Locate and identify every blood parasite.
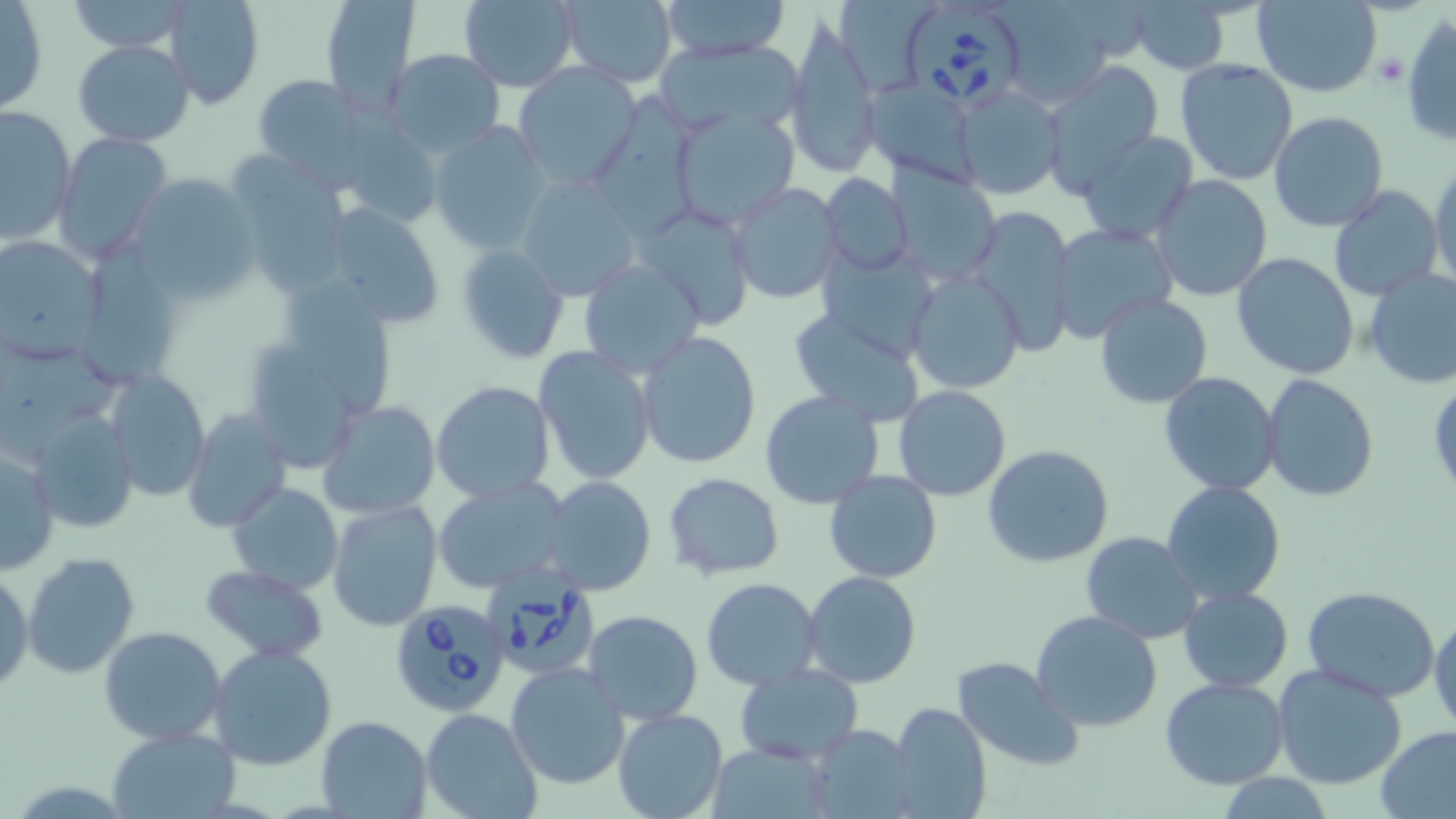
Approximate bounding boxes as [x1, y1, x2, y2] in pixels.
Babesia divergens-infected red blood cells: [906, 3, 1028, 113], [479, 568, 598, 681], [391, 599, 514, 718].
No Plasmodium falciparum, Plasmodium ovale, Plasmodium malariae, Plasmodium vivax, or Trypanosoma brucei observed.

Summary:
  - Uninfected red blood cell locations: [63, 0, 192, 54], [162, 0, 264, 110], [318, 0, 421, 117], [458, 0, 579, 90], [556, 0, 680, 89], [657, 0, 789, 60], [1251, 0, 1382, 97], [992, 1, 1120, 108], [1130, 1, 1229, 74], [1, 2, 48, 116], [782, 15, 883, 178], [1402, 15, 1456, 149], [656, 38, 806, 138], [72, 40, 194, 147], [386, 49, 506, 158], [403, 50, 527, 246], [1174, 59, 1298, 186], [1040, 61, 1164, 196], [513, 62, 640, 191], [249, 73, 369, 180], [865, 87, 992, 186], [953, 88, 1062, 199], [598, 92, 702, 241], [1, 104, 77, 244], [669, 108, 801, 229], [1268, 110, 1390, 232], [429, 121, 554, 254], [1076, 129, 1199, 245], [52, 132, 172, 263], [234, 152, 354, 296], [1429, 160, 1456, 289], [128, 172, 259, 304], [515, 173, 641, 300], [819, 174, 914, 277], [1151, 175, 1272, 300], [727, 182, 845, 305], [1328, 185, 1443, 301], [313, 199, 446, 330], [633, 200, 755, 329], [965, 205, 1078, 358], [1049, 223, 1178, 340], [0, 235, 107, 363], [455, 243, 570, 364], [818, 250, 943, 363], [1232, 252, 1360, 380], [576, 256, 708, 380], [1362, 266, 1456, 388], [904, 268, 1026, 394], [289, 285, 393, 419], [1094, 293, 1214, 408], [786, 305, 929, 425], [636, 330, 762, 469], [242, 335, 354, 473], [534, 346, 655, 484], [104, 370, 210, 500], [1159, 372, 1283, 495], [1260, 373, 1379, 500], [430, 381, 556, 503], [894, 385, 1011, 500], [760, 390, 884, 509], [320, 398, 441, 519], [181, 407, 291, 531], [24, 408, 140, 535], [1, 443, 61, 574], [983, 445, 1115, 568], [824, 469, 942, 583], [661, 471, 785, 580], [431, 476, 572, 595], [541, 476, 657, 596], [1161, 481, 1288, 607], [227, 482, 344, 595], [328, 500, 445, 632], [1079, 531, 1203, 643], [23, 552, 141, 679], [199, 563, 328, 664], [0, 568, 33, 697], [804, 570, 922, 690], [701, 577, 823, 690], [1302, 584, 1440, 701], [1177, 587, 1293, 693], [583, 610, 703, 724], [1031, 610, 1165, 734], [1430, 613, 1456, 735], [100, 627, 227, 746], [209, 643, 339, 771], [951, 656, 1085, 771], [505, 662, 632, 790], [1271, 663, 1407, 789], [733, 665, 863, 765], [1159, 676, 1289, 788], [885, 702, 992, 819], [420, 706, 542, 819], [612, 709, 727, 819], [315, 715, 432, 817], [802, 725, 918, 819], [106, 726, 239, 817], [1375, 726, 1456, 819], [702, 742, 836, 818]
  - Platelet locations: [1375, 51, 1407, 86]
  - Slide-level diagnosis: Babesia divergens
  - Image size: 1456×819 pixels
  - Preparation: thin blood smear
  - Magnification: 1000x
  - Field of view: one of a larger specimen
  - Stain: May-Grünwald-Giemsa
  - Modality: light microscopy